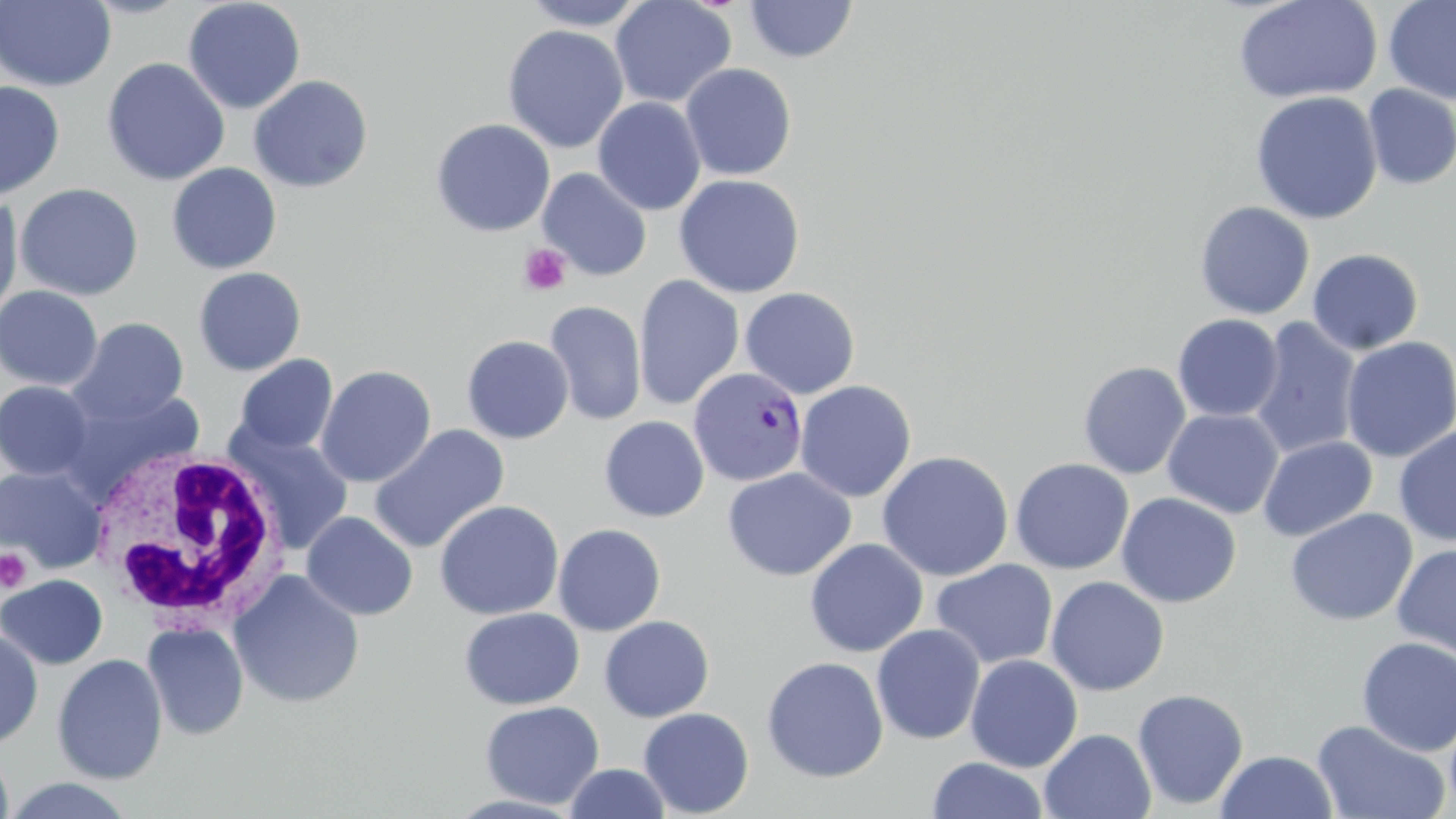

Plasmodium vivax-infected red blood cell locations = approximate bounding boxes as (x1,y1)-(x2,y2) corner pairs in pixels: (688,367)-(808,487)
slide-level diagnosis = Plasmodium vivax
platelet locations = approximate bounding boxes as (x1,y1)-(x2,y2) corner pairs in pixels: (518,244)-(572,296), (0,547)-(32,594)
stain = May-Grünwald-Giemsa
field of view = single
uninfected red blood cell locations = approximate bounding boxes as (x1,y1)-(x2,y2) corner pairs in pixels: (0,0)-(116,92), (182,0)-(306,115), (519,0)-(647,30), (610,0)-(736,109), (1231,0)-(1383,105), (1383,0)-(1456,106), (743,1)-(858,64), (502,24)-(629,154), (101,57)-(230,186), (680,63)-(797,181), (248,75)-(373,193), (0,80)-(65,201), (1362,84)-(1456,190), (1250,90)-(1383,225), (592,97)-(706,215), (430,118)-(556,237), (166,162)-(282,274), (538,167)-(652,281), (673,173)-(805,299), (15,183)-(143,301), (0,192)-(24,325), (1194,201)-(1315,320), (1306,247)-(1424,355), (193,267)-(307,376), (634,275)-(744,410), (0,285)-(103,391), (739,287)-(860,399), (544,301)-(647,426), (1172,314)-(1283,422), (69,317)-(189,425), (1249,318)-(1362,459), (461,335)-(574,444), (1340,336)-(1456,463), (233,354)-(339,456), (1078,362)-(1191,480), (316,365)-(436,487), (0,380)-(95,481), (794,380)-(917,502), (60,387)-(207,500), (1162,408)-(1284,519), (600,416)-(709,522), (368,425)-(510,554), (1393,425)-(1456,547), (229,428)-(354,555), (1257,435)-(1378,542), (1174,440)-(1352,583), (876,450)-(1014,581), (1011,458)-(1134,575), (0,466)-(106,574), (723,467)-(856,581), (1115,492)-(1242,608), (434,500)-(564,620), (1285,508)-(1417,627), (301,512)-(418,621), (552,524)-(666,636), (805,537)-(928,658), (1392,542)-(1456,661), (930,559)-(1058,670), (228,569)-(365,709), (0,575)-(108,670), (1046,576)-(1169,697), (459,607)-(584,710), (599,615)-(715,723), (142,621)-(249,740), (871,624)-(985,745), (0,627)-(44,748), (1356,637)-(1456,756), (52,653)-(167,784), (965,654)-(1083,772), (761,656)-(889,783), (1132,688)-(1249,811), (480,700)-(604,809), (639,707)-(754,817), (1445,709)-(1456,816), (1311,720)-(1452,819), (1039,729)-(1156,819), (0,743)-(14,819), (1216,749)-(1338,818), (927,756)-(1049,818), (564,763)-(671,818), (1,777)-(139,818)
modality = optical microscopy
image size = 1456×819 pixels
magnification = 1000x
preparation = thin blood smear
white blood cell locations = approximate bounding boxes as (x1,y1)-(x2,y2) corner pairs in pixels: (86,447)-(286,628)